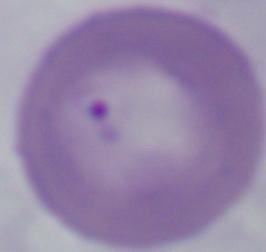
modality = micrograph
magnification = 1000x
identification = Babesia